Locate and identify every blood parasite.
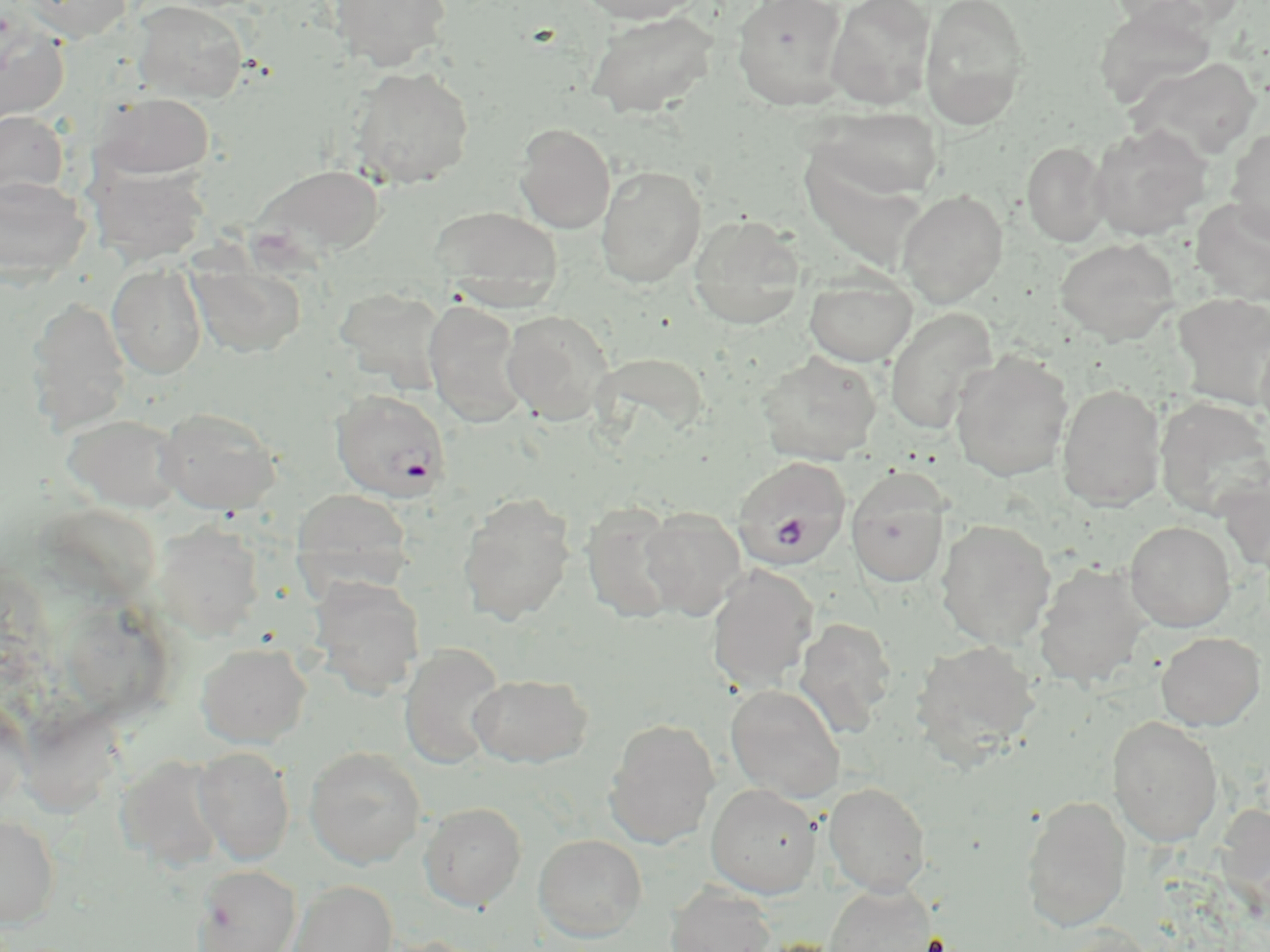
Approximate bounding boxes as named x1/y1/x2/y2 corners in pixels.
Plasmodium falciparum-infected red blood cells: (x1=329, y1=389, x2=452, y2=503), (x1=731, y1=456, x2=852, y2=568).
No Plasmodium ovale, Plasmodium malariae, Plasmodium vivax, Babesia divergens, or Trypanosoma brucei observed.

Summary:
  - Uninfected red blood cell locations: (x1=18, y1=0, x2=132, y2=43), (x1=133, y1=0, x2=248, y2=103), (x1=327, y1=0, x2=452, y2=70), (x1=573, y1=0, x2=705, y2=24), (x1=732, y1=0, x2=848, y2=110), (x1=826, y1=0, x2=937, y2=109), (x1=920, y1=0, x2=1031, y2=129), (x1=1093, y1=6, x2=1216, y2=110), (x1=586, y1=10, x2=718, y2=118), (x1=0, y1=12, x2=70, y2=126), (x1=1129, y1=56, x2=1261, y2=160), (x1=348, y1=65, x2=474, y2=188), (x1=95, y1=92, x2=214, y2=179), (x1=815, y1=106, x2=943, y2=200), (x1=0, y1=111, x2=68, y2=197), (x1=1090, y1=122, x2=1212, y2=240), (x1=514, y1=124, x2=616, y2=233), (x1=1226, y1=126, x2=1270, y2=244), (x1=1021, y1=141, x2=1110, y2=247), (x1=251, y1=163, x2=385, y2=258), (x1=90, y1=164, x2=208, y2=263), (x1=596, y1=164, x2=707, y2=287), (x1=0, y1=176, x2=90, y2=284), (x1=897, y1=189, x2=1008, y2=307), (x1=1191, y1=198, x2=1270, y2=306), (x1=431, y1=205, x2=564, y2=309), (x1=688, y1=214, x2=806, y2=329), (x1=1054, y1=237, x2=1180, y2=346), (x1=188, y1=257, x2=306, y2=359), (x1=107, y1=262, x2=207, y2=379), (x1=804, y1=274, x2=917, y2=367), (x1=334, y1=286, x2=447, y2=391), (x1=1172, y1=292, x2=1270, y2=411), (x1=26, y1=295, x2=131, y2=435), (x1=423, y1=299, x2=528, y2=427), (x1=885, y1=307, x2=997, y2=434), (x1=500, y1=309, x2=615, y2=424), (x1=1256, y1=329, x2=1270, y2=446), (x1=950, y1=350, x2=1073, y2=482), (x1=756, y1=351, x2=882, y2=466), (x1=1057, y1=384, x2=1166, y2=510), (x1=1155, y1=397, x2=1270, y2=520), (x1=156, y1=406, x2=281, y2=515), (x1=62, y1=413, x2=186, y2=513), (x1=845, y1=469, x2=951, y2=588), (x1=292, y1=489, x2=413, y2=593), (x1=458, y1=492, x2=576, y2=625), (x1=580, y1=502, x2=682, y2=622), (x1=638, y1=506, x2=746, y2=619), (x1=936, y1=518, x2=1056, y2=648), (x1=1124, y1=520, x2=1236, y2=631), (x1=154, y1=522, x2=264, y2=638), (x1=1033, y1=561, x2=1152, y2=689), (x1=706, y1=564, x2=818, y2=693), (x1=309, y1=575, x2=426, y2=699), (x1=794, y1=618, x2=897, y2=737), (x1=1156, y1=631, x2=1265, y2=731), (x1=911, y1=639, x2=1041, y2=762), (x1=195, y1=642, x2=311, y2=747), (x1=399, y1=643, x2=506, y2=769), (x1=469, y1=673, x2=593, y2=768), (x1=725, y1=684, x2=845, y2=803), (x1=0, y1=696, x2=30, y2=815), (x1=1106, y1=715, x2=1223, y2=846), (x1=604, y1=717, x2=720, y2=848), (x1=193, y1=746, x2=295, y2=865), (x1=304, y1=746, x2=426, y2=869), (x1=116, y1=754, x2=227, y2=871), (x1=823, y1=781, x2=931, y2=896), (x1=706, y1=783, x2=821, y2=898), (x1=1020, y1=795, x2=1130, y2=932), (x1=419, y1=802, x2=527, y2=911), (x1=0, y1=814, x2=61, y2=927), (x1=534, y1=834, x2=647, y2=941), (x1=192, y1=864, x2=301, y2=952), (x1=288, y1=880, x2=397, y2=952), (x1=665, y1=883, x2=777, y2=952), (x1=824, y1=883, x2=937, y2=952), (x1=1050, y1=926, x2=1164, y2=952), (x1=372, y1=935, x2=495, y2=952)
  - Slide-level diagnosis: Plasmodium falciparum
  - Preparation: thin blood smear
  - Magnification: 1000x
  - Stain: May-Grünwald-Giemsa
  - Modality: optical microscopy
  - Field of view: single
  - Image size: 1270×952 pixels